Describe the morphology of the erythrocytes.
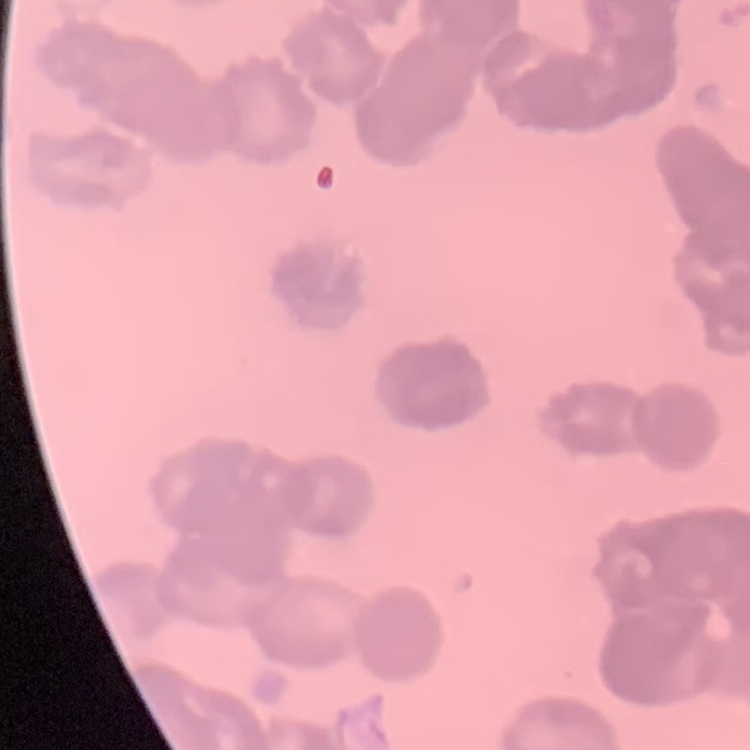
Rouleaux formation.

One tile cut from a larger photomicrograph. Thin blood smear. Stained with either Field's or Giemsa.